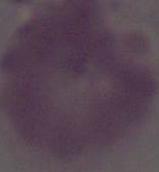

Summary:
  - Magnification: 1000x
  - Identification: erythrocyte
  - Modality: micrograph